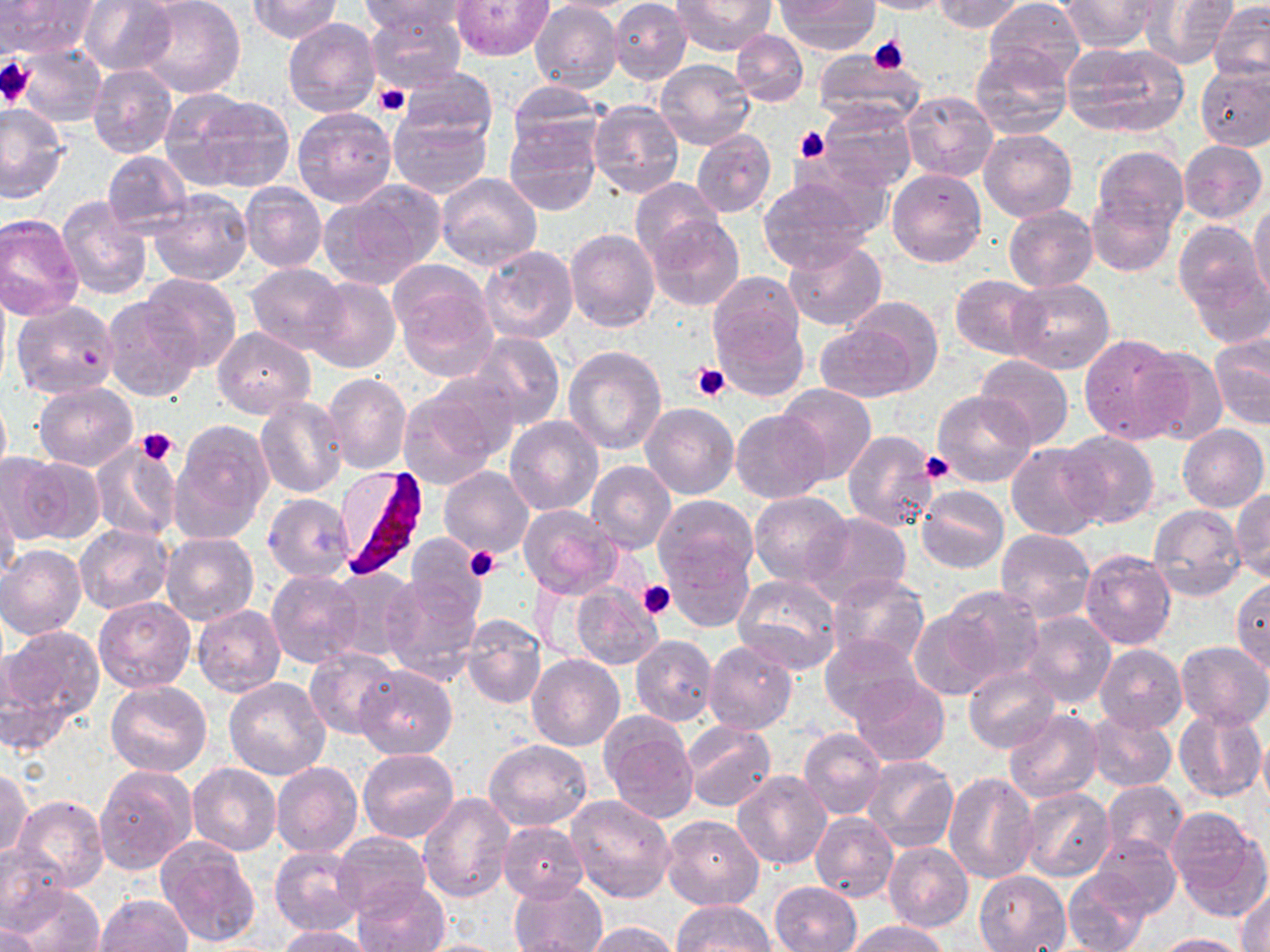
slide-level diagnosis = Plasmodium falciparum
uninfected red blood cell locations = approximate bounding boxes as (x1,y1)-(x2,y2) corner pairs in pixels: (2,0)-(96,57), (77,0)-(178,75), (134,0)-(246,99), (246,0)-(342,42), (362,0)-(468,39), (452,0)-(553,59), (542,0)-(647,13), (673,0)-(775,56), (857,0)-(951,14), (932,0)-(1025,33), (986,0)-(1085,88), (1060,0)-(1160,52), (1137,0)-(1235,69), (610,1)-(692,83), (777,1)-(879,55), (530,2)-(621,94), (1208,2)-(1270,83), (366,10)-(466,93), (282,18)-(381,118), (732,29)-(808,106), (288,40)-(387,188), (1062,41)-(1190,138), (16,43)-(107,126), (969,45)-(1071,140), (814,48)-(924,125), (654,58)-(754,149), (87,64)-(177,158), (1196,64)-(1270,150), (399,67)-(499,144), (508,81)-(608,155), (899,90)-(997,184), (173,92)-(295,192), (588,100)-(684,199), (816,101)-(917,191), (0,103)-(66,202), (292,106)-(396,207), (389,113)-(491,199), (503,117)-(601,216), (978,129)-(1077,222), (692,130)-(776,217), (1177,140)-(1267,224), (1092,146)-(1189,236), (102,150)-(191,235), (886,168)-(987,268), (434,172)-(542,272), (755,174)-(880,274), (630,177)-(723,265), (239,182)-(326,273), (320,182)-(445,289), (147,189)-(252,285), (1084,192)-(1176,277), (56,196)-(152,299), (1249,203)-(1270,304), (1003,205)-(1098,292), (0,214)-(85,320), (646,215)-(743,312), (1173,220)-(1261,309), (564,227)-(659,332), (782,239)-(887,330), (478,246)-(579,345), (1187,260)-(1270,347), (245,262)-(347,354), (389,263)-(497,380), (708,270)-(806,372), (140,273)-(242,370), (950,274)-(1046,358), (306,277)-(401,374), (1006,279)-(1113,375), (102,295)-(203,404), (844,296)-(944,394), (11,300)-(118,399), (1041,305)-(1154,432), (816,321)-(923,402), (212,326)-(315,418), (466,333)-(565,430), (1078,333)-(1190,443), (1209,335)-(1269,431), (1137,345)-(1231,445), (562,346)-(667,455), (975,354)-(1074,449), (425,372)-(522,463), (323,373)-(413,474), (33,381)-(138,470), (774,384)-(876,483), (0,386)-(12,489), (397,389)-(499,493), (931,391)-(1038,489), (255,398)-(349,498), (641,402)-(736,498), (731,409)-(831,503), (505,416)-(602,515), (168,422)-(273,541), (1177,424)-(1268,512), (842,430)-(942,533), (1059,433)-(1160,527), (1006,442)-(1106,539), (89,443)-(181,543), (17,456)-(105,544), (587,460)-(677,553), (439,466)-(535,559), (916,484)-(1009,573), (0,487)-(21,583), (1232,488)-(1270,581), (750,491)-(853,586), (263,493)-(355,581), (653,495)-(759,589), (516,504)-(624,600), (1149,504)-(1245,602), (802,512)-(912,607), (73,524)-(173,613), (994,528)-(1094,624), (161,533)-(259,627), (404,535)-(488,621), (666,541)-(753,632), (1,544)-(86,639), (1078,549)-(1176,650), (327,568)-(419,664), (266,570)-(364,669), (827,572)-(931,671), (381,573)-(484,684), (733,574)-(842,675), (1230,577)-(1270,672), (570,585)-(664,670), (941,586)-(1046,688), (93,597)-(196,693), (958,601)-(1097,703), (193,605)-(285,697), (1018,610)-(1117,710), (461,611)-(546,710), (910,612)-(998,700), (2,624)-(103,724), (631,635)-(718,727), (819,635)-(923,722), (705,640)-(798,735), (1175,641)-(1270,729), (1095,644)-(1186,733), (305,646)-(402,740), (527,655)-(624,752), (355,664)-(457,758), (964,667)-(1059,753), (847,675)-(949,766), (225,676)-(331,779), (106,680)-(211,777), (1173,707)-(1267,803), (1003,709)-(1103,803), (1084,711)-(1177,792), (599,714)-(698,824), (682,721)-(775,811), (800,727)-(886,819), (1258,732)-(1270,817), (483,740)-(591,831), (358,749)-(458,844), (862,755)-(959,852), (271,761)-(363,858), (188,763)-(281,855), (95,764)-(197,875), (0,766)-(32,861), (733,769)-(832,870), (942,773)-(1040,884), (1101,781)-(1188,862), (1019,787)-(1114,882), (418,793)-(513,903), (566,794)-(677,902), (12,795)-(108,893), (1168,810)-(1268,919), (811,812)-(898,902), (660,815)-(764,911), (499,820)-(589,902), (332,832)-(431,916), (1090,833)-(1180,918), (156,836)-(260,947), (883,841)-(973,931), (0,842)-(68,927), (270,846)-(366,936), (974,870)-(1071,951), (1063,870)-(1151,951), (509,878)-(608,952), (354,879)-(448,952), (768,881)-(862,951), (7,883)-(105,952), (1236,886)-(1270,951), (92,895)-(192,952), (674,901)-(775,951), (843,920)-(949,952), (585,921)-(680,952), (0,922)-(43,952), (276,925)-(378,952), (1149,933)-(1250,952), (410,938)-(521,952)
Plasmodium falciparum-infected red blood cell locations = approximate bounding boxes as (x1,y1)-(x2,y2) corner pairs in pixels: (334,466)-(434,582)
modality = optical microscopy
magnification = 1000x
image size = 1270×952 pixels
stain = May-Grünwald-Giemsa
field of view = one of a larger specimen
platelet locations = approximate bounding boxes as (x1,y1)-(x2,y2) corner pairs in pixels: (867,36)-(910,72), (0,55)-(36,109), (374,83)-(411,117), (794,124)-(830,164), (691,362)-(730,401), (135,428)-(179,467), (919,452)-(951,483), (466,548)-(501,582), (637,580)-(675,619)
preparation = thin blood smear